Comment on the morphology of the erythrocytes.
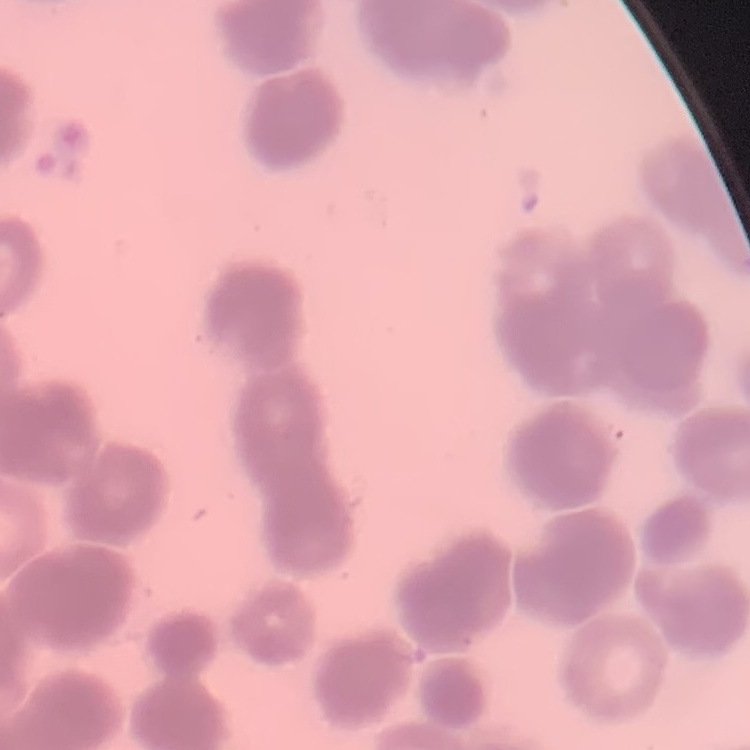

Rouleaux formation.

Field's or Giemsa stain. One tile cut from a larger photomicrograph. Thin blood film.